Point out each Plasmodium parasite.
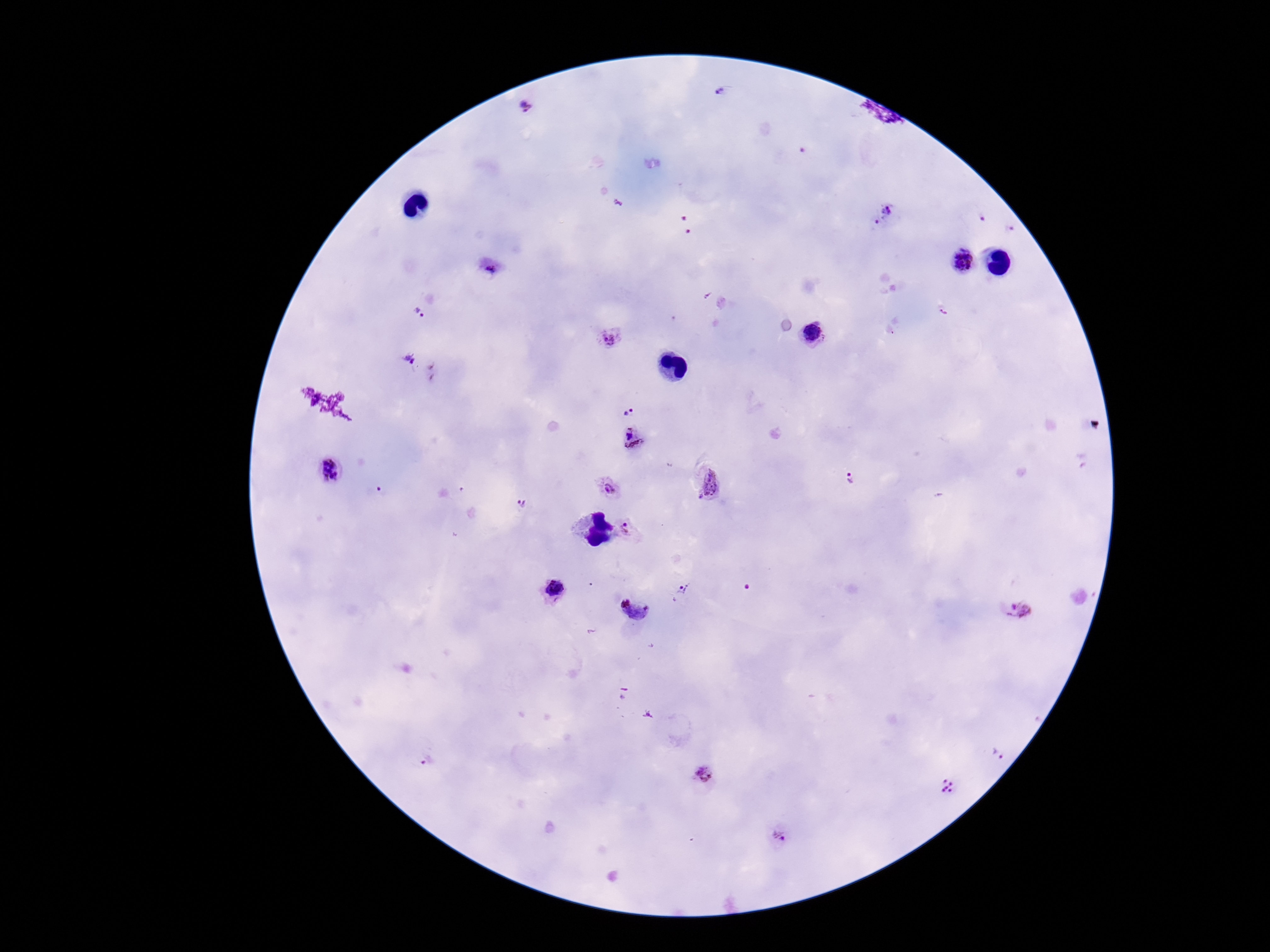

Approximate centers as {x, y} in pixels.
Plasmodium parasites: {722, 93}, {527, 105}, {890, 210}, {982, 218}, {877, 223}, {1012, 230}, {964, 264}, {490, 270}, {420, 314}, {812, 335}, {609, 338}, {411, 361}, {626, 407}, {632, 439}, {330, 471}, {851, 478}, {713, 486}, {384, 490}, {611, 490}, {521, 504}, {628, 532}, {683, 591}, {554, 592}, {1015, 609}, {638, 612}, {1000, 752}, {426, 760}, {706, 776}, {949, 789}, {783, 837}.

Summary:
  - Magnification: 100x
  - Stain: Giemsa
  - Field of view: single
  - Image size: 1270×952 pixels
  - Patient malaria status: infected
  - Capture: smartphone camera through the microscope eyepiece
  - Preparation: thick blood film